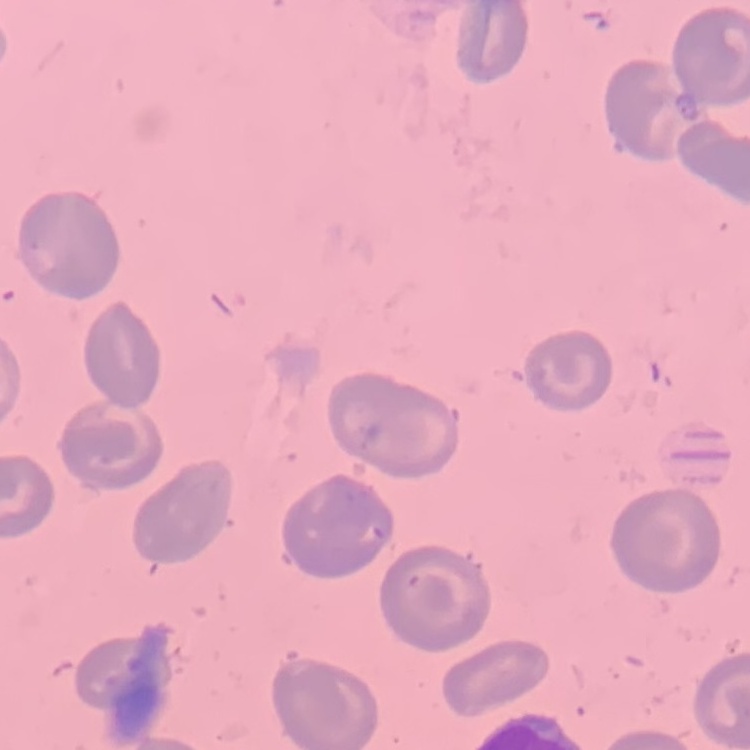

The red blood cells exhibit no rouleaux formation. One tile cut from a larger photomicrograph. Thin blood smear. Stained with either Field's or Giemsa.